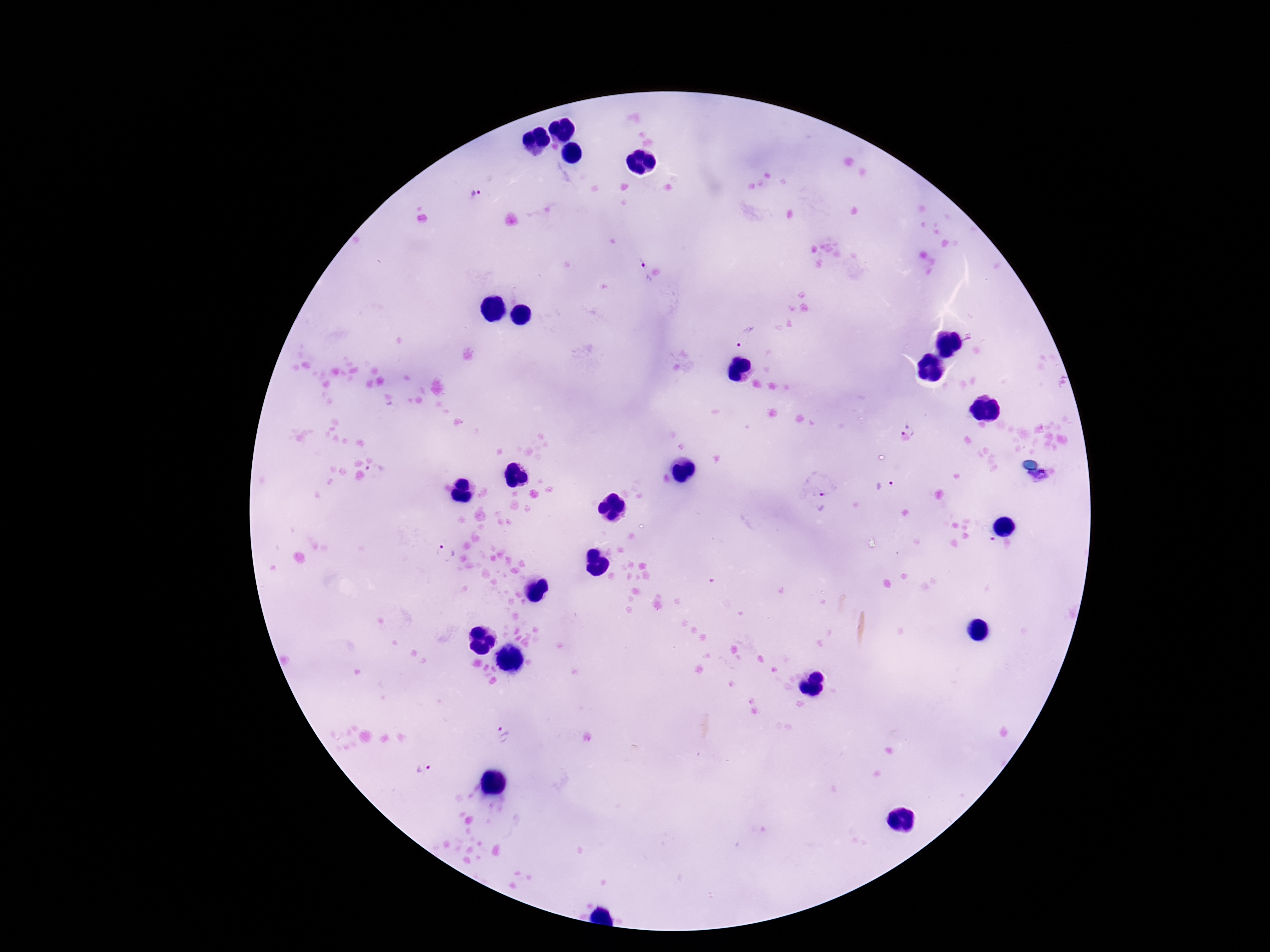
Approximate object centers, in pixels from the top-left corner.
Summary:
  - Plasmodium parasite locations: (x=476, y=194), (x=638, y=272), (x=746, y=335), (x=969, y=336), (x=903, y=426), (x=375, y=470), (x=1040, y=478), (x=884, y=485), (x=822, y=501), (x=987, y=536), (x=446, y=552), (x=502, y=732), (x=420, y=768)
  - Patient malaria status: infected
  - Capture: smartphone camera through the microscope eyepiece
  - Preparation: thick blood smear
  - Magnification: 100x
  - Field of view: single
  - Stain: Giemsa
  - Image size: 1270×952 pixels